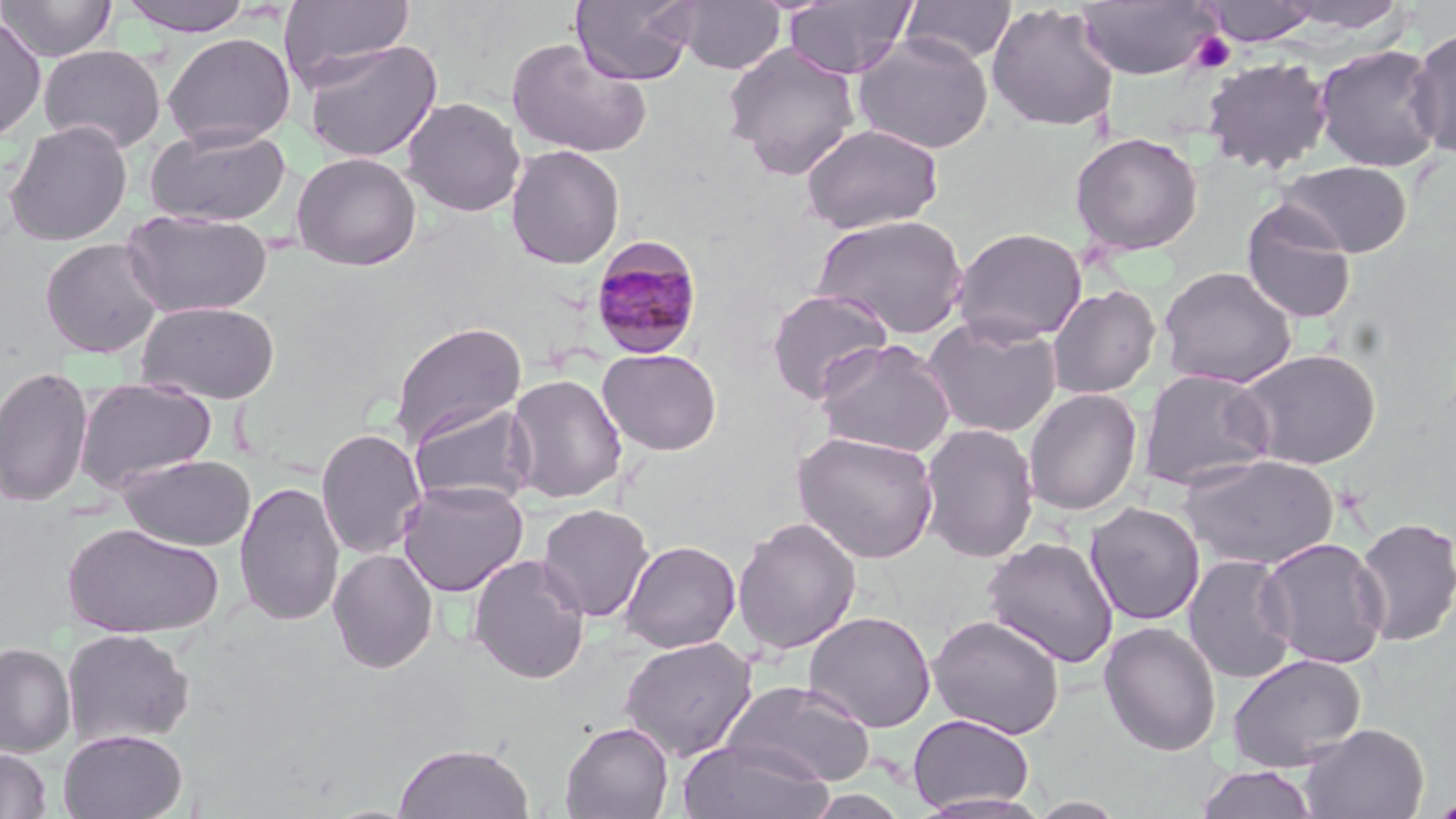

Summary:
  - Coordinate format: approximate bounding boxes as named x1/y1/x2/y2 corners in pixels
  - Plasmodium malariae-infected red blood cell locations: (x1=588, y1=236, x2=705, y2=360)
  - Uninfected red blood cell locations: (x1=0, y1=0, x2=116, y2=61), (x1=118, y1=0, x2=256, y2=36), (x1=277, y1=0, x2=415, y2=89), (x1=571, y1=0, x2=699, y2=86), (x1=672, y1=0, x2=786, y2=75), (x1=783, y1=0, x2=917, y2=79), (x1=901, y1=0, x2=1016, y2=65), (x1=1200, y1=0, x2=1320, y2=45), (x1=1075, y1=1, x2=1219, y2=80), (x1=1276, y1=1, x2=1409, y2=34), (x1=986, y1=2, x2=1119, y2=132), (x1=0, y1=17, x2=47, y2=142), (x1=1406, y1=27, x2=1456, y2=160), (x1=163, y1=32, x2=296, y2=150), (x1=853, y1=32, x2=995, y2=154), (x1=506, y1=37, x2=652, y2=159), (x1=301, y1=38, x2=442, y2=163), (x1=722, y1=42, x2=861, y2=180), (x1=1312, y1=43, x2=1445, y2=173), (x1=38, y1=44, x2=166, y2=153), (x1=1201, y1=56, x2=1333, y2=174), (x1=402, y1=97, x2=526, y2=217), (x1=4, y1=120, x2=132, y2=246), (x1=802, y1=122, x2=943, y2=233), (x1=144, y1=124, x2=292, y2=227), (x1=1069, y1=131, x2=1204, y2=256), (x1=506, y1=144, x2=625, y2=270), (x1=292, y1=152, x2=422, y2=271), (x1=1278, y1=160, x2=1413, y2=258), (x1=1241, y1=200, x2=1358, y2=325), (x1=121, y1=209, x2=273, y2=318), (x1=812, y1=213, x2=969, y2=339), (x1=951, y1=227, x2=1088, y2=345), (x1=40, y1=238, x2=164, y2=358), (x1=1159, y1=266, x2=1297, y2=389), (x1=1047, y1=284, x2=1161, y2=399), (x1=765, y1=289, x2=894, y2=405), (x1=138, y1=300, x2=281, y2=404), (x1=922, y1=315, x2=1063, y2=437), (x1=390, y1=321, x2=526, y2=447), (x1=816, y1=338, x2=956, y2=457), (x1=1232, y1=346, x2=1383, y2=471), (x1=597, y1=348, x2=722, y2=456), (x1=0, y1=365, x2=94, y2=508), (x1=1138, y1=369, x2=1275, y2=493), (x1=506, y1=373, x2=628, y2=504), (x1=74, y1=379, x2=218, y2=493), (x1=1023, y1=388, x2=1142, y2=516), (x1=407, y1=402, x2=536, y2=509), (x1=918, y1=423, x2=1040, y2=564), (x1=315, y1=426, x2=428, y2=560), (x1=793, y1=430, x2=939, y2=563), (x1=1179, y1=453, x2=1340, y2=570), (x1=118, y1=454, x2=256, y2=551), (x1=397, y1=479, x2=529, y2=597), (x1=234, y1=480, x2=345, y2=627), (x1=1085, y1=502, x2=1205, y2=626), (x1=536, y1=503, x2=655, y2=623), (x1=1353, y1=515, x2=1456, y2=648), (x1=732, y1=517, x2=862, y2=655), (x1=64, y1=523, x2=224, y2=638), (x1=981, y1=536, x2=1120, y2=669), (x1=1256, y1=537, x2=1390, y2=670), (x1=619, y1=540, x2=741, y2=653), (x1=328, y1=548, x2=439, y2=673), (x1=468, y1=553, x2=591, y2=684), (x1=1183, y1=554, x2=1298, y2=685), (x1=803, y1=610, x2=937, y2=733), (x1=928, y1=613, x2=1066, y2=739), (x1=1098, y1=621, x2=1222, y2=756), (x1=62, y1=628, x2=196, y2=748), (x1=618, y1=636, x2=757, y2=761), (x1=0, y1=642, x2=76, y2=757), (x1=1226, y1=653, x2=1367, y2=772), (x1=722, y1=679, x2=876, y2=788), (x1=907, y1=713, x2=1035, y2=813), (x1=560, y1=721, x2=674, y2=819), (x1=1298, y1=723, x2=1429, y2=818), (x1=58, y1=729, x2=188, y2=819), (x1=677, y1=738, x2=835, y2=819), (x1=393, y1=743, x2=535, y2=819), (x1=0, y1=746, x2=52, y2=819), (x1=1194, y1=765, x2=1320, y2=819), (x1=909, y1=792, x2=1054, y2=819), (x1=1424, y1=795, x2=1456, y2=818)
  - Platelet locations: (x1=1188, y1=31, x2=1236, y2=75)
  - Slide-level diagnosis: Plasmodium malariae
  - Field of view: single
  - Image size: 1456×819 pixels
  - Modality: optical microscopy
  - Stain: May-Grünwald-Giemsa
  - Preparation: thin blood film
  - Magnification: 1000x